Assess this cell for malaria.
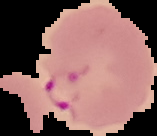

It is parasitized.

preparation: thin blood film
image_size: 157×136 pixels
image_type: cell region segmented out of the field of view; surrounding area masked to black